Classify this cell by malaria status.
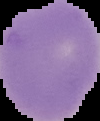
It is uninfected.

From a thin blood film. Image is 100×121 pixels. Segmented cell region on a black background.